Give the position of every malaria parasite.
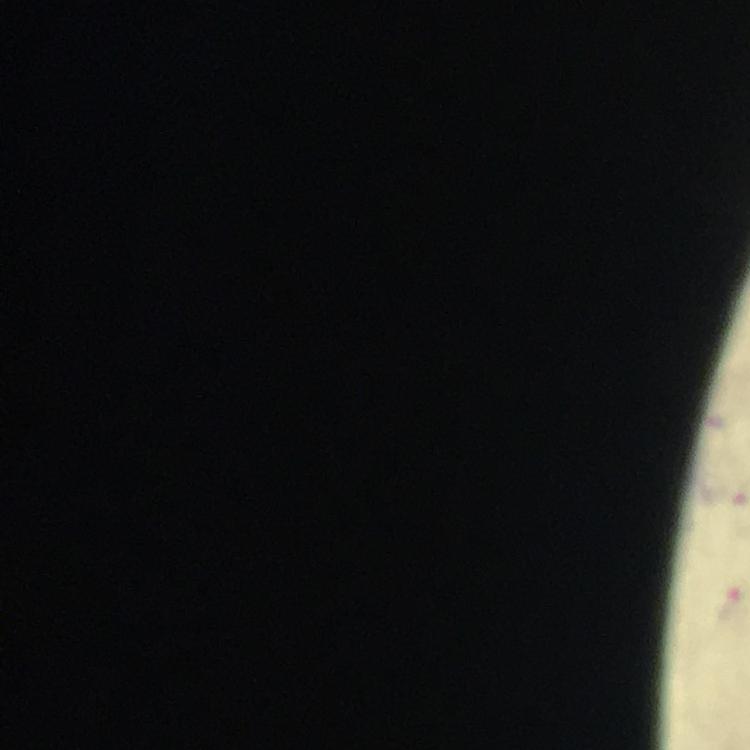

Approximate centers as [x, y] in pixels.
Malaria parasites: [730, 602].

Summary:
  - Image size: 750×750 pixels
  - Magnification: 100x
  - Capture: smartphone photograph through a microscope
  - Cropped from: a single field of view
  - Preparation: thick blood smear
  - Stain: Giemsa
  - Context: from a diagnostic examination for malaria
  - Immersion oil: applied